Name the parasite shown.
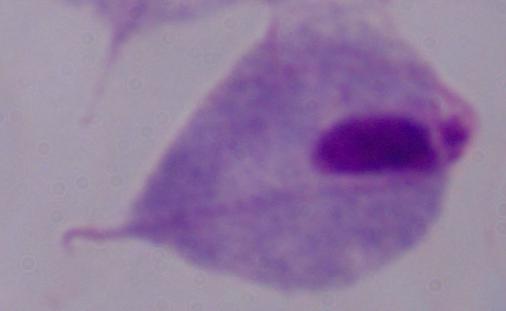
This is a trichomonad.

modality = photomicrograph
magnification = 1000x